Identify the blood parasite species.
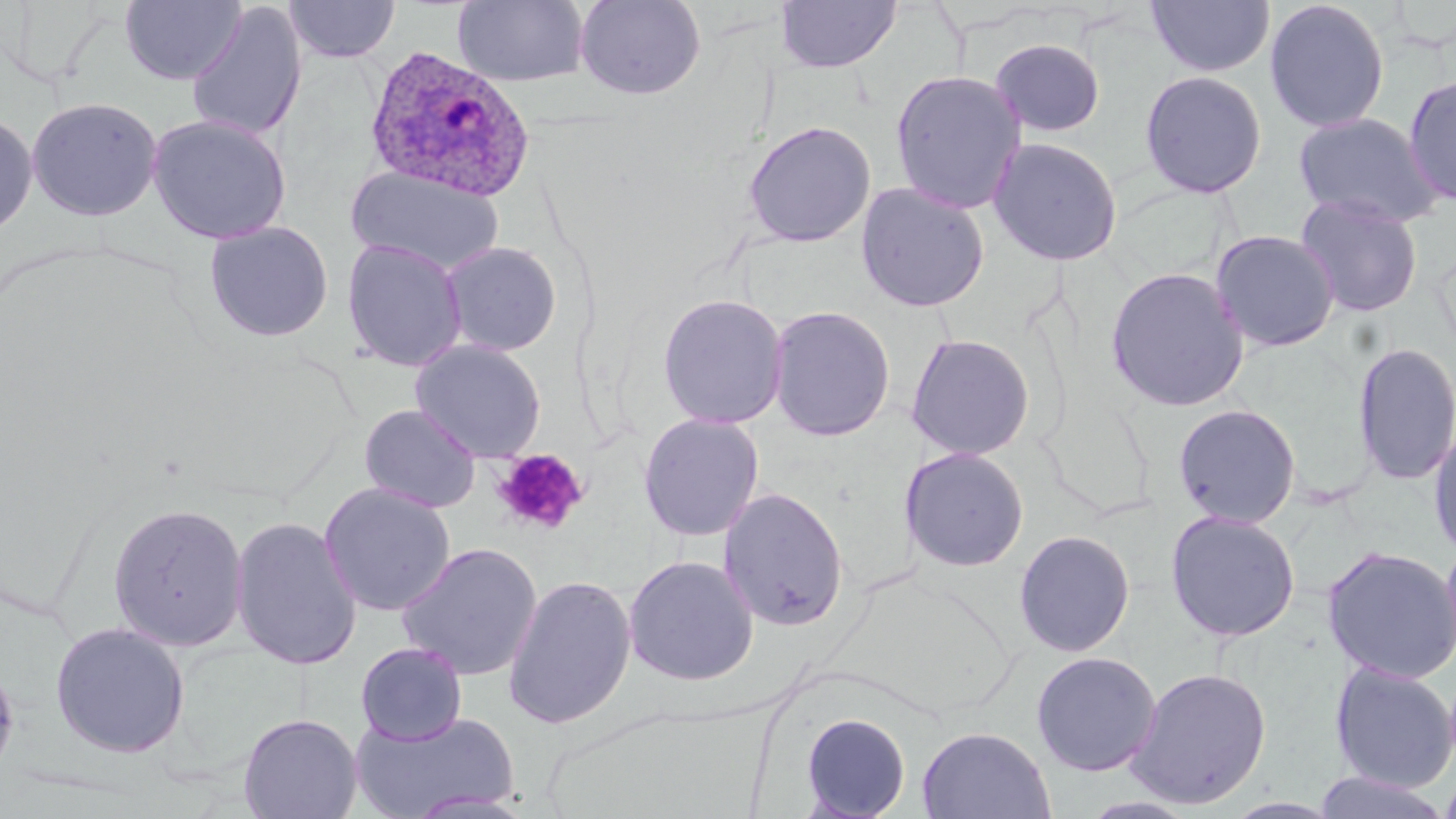
Plasmodium ovale.

Approximate bounding boxes as (x1, y1, x2, y2) in pixels. Plasmodium ovale-infected red blood cell locations: (364, 45, 536, 203). Uninfected red blood cell locations: (120, 0, 245, 86), (283, 0, 401, 64), (453, 0, 590, 88), (574, 0, 706, 100), (1146, 0, 1275, 77), (1264, 0, 1390, 134), (775, 1, 901, 73), (185, 4, 308, 142), (989, 37, 1107, 138), (890, 68, 1027, 215), (1138, 70, 1268, 199), (1402, 73, 1456, 206), (26, 95, 163, 221), (0, 111, 38, 239), (1292, 111, 1445, 228), (146, 113, 292, 244), (742, 120, 876, 248), (987, 136, 1124, 266), (346, 166, 504, 276), (855, 181, 990, 312), (1294, 193, 1424, 317), (203, 221, 334, 342), (1209, 229, 1341, 353), (341, 238, 467, 372), (439, 241, 563, 357), (1105, 266, 1250, 413), (656, 293, 790, 429), (768, 305, 896, 441), (905, 333, 1035, 460), (410, 339, 547, 463), (1352, 341, 1456, 487), (358, 403, 483, 513), (1172, 403, 1302, 528), (638, 413, 765, 542), (1428, 422, 1456, 561), (899, 446, 1030, 572), (319, 483, 456, 616), (718, 486, 850, 631), (108, 501, 249, 651), (1164, 510, 1301, 642), (229, 516, 362, 670), (1014, 529, 1135, 658), (1440, 535, 1456, 668), (396, 542, 543, 681), (1321, 545, 1456, 684), (622, 554, 760, 686), (502, 573, 637, 730), (49, 621, 191, 759), (356, 642, 468, 745), (1031, 651, 1161, 777), (0, 655, 19, 789), (1328, 661, 1456, 793), (1125, 665, 1272, 810), (351, 709, 518, 818), (800, 712, 911, 819), (238, 713, 362, 819), (917, 726, 1055, 819), (1438, 765, 1456, 819), (1312, 771, 1451, 818). Platelet locations: (492, 449, 589, 535). Single field of view. Thin blood smear. 1000x magnification. Image is 1456×819 pixels. May-Grünwald-Giemsa stain. Light microscopy.